Describe the morphology of the erythrocytes.
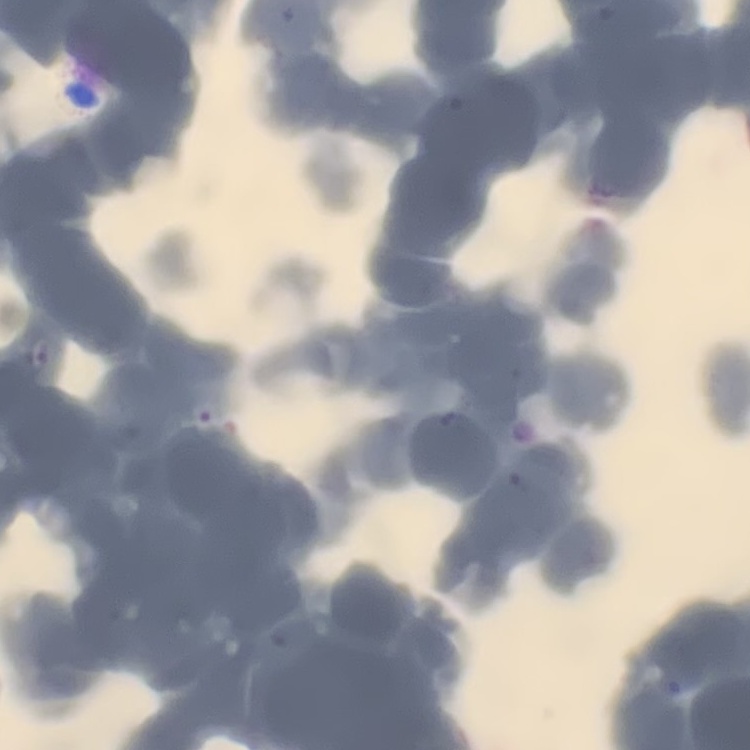
Rouleaux formation.

{
  "image_type": "one tile cut from a larger photomicrograph",
  "stain": "Field's or Giemsa",
  "preparation": "thin peripheral smear"
}